Describe the morphology of the red blood cells.
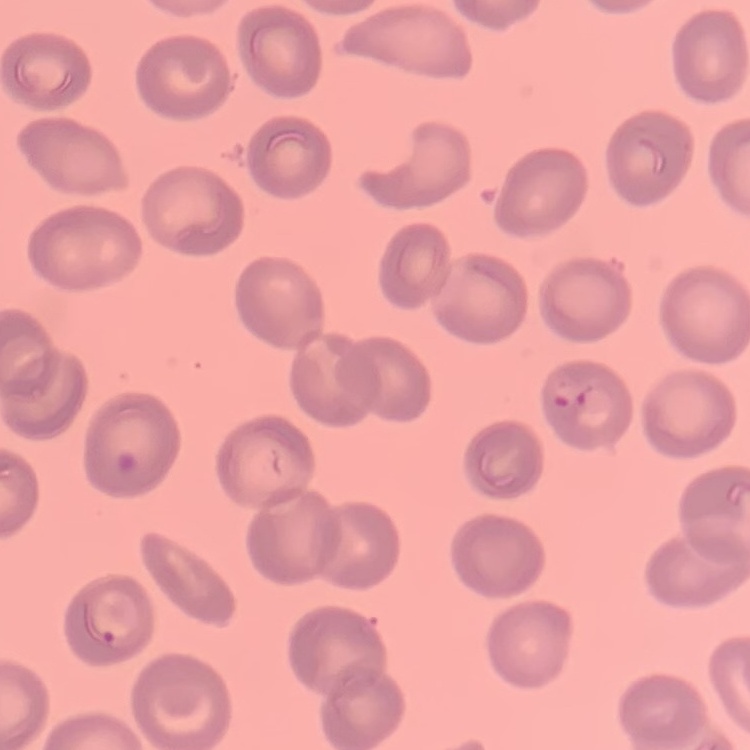

No rouleaux formation.

Summary:
  - Preparation: thin blood smear
  - Image type: one tile cut from a larger photomicrograph
  - Stain: Field's or Giemsa